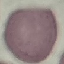
result = no malaria parasites seen
capture = smartphone through the microscope eyepiece
image type = cell patch, automatically extracted from a larger field of view and resized to 64 × 64 pixels
preparation = thin smear
stain = Giemsa